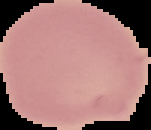
result = negative for Plasmodium parasites
image size = 151×130 pixels
image type = cell region segmented out of the field of view; surrounding area masked to black
preparation = thin blood film